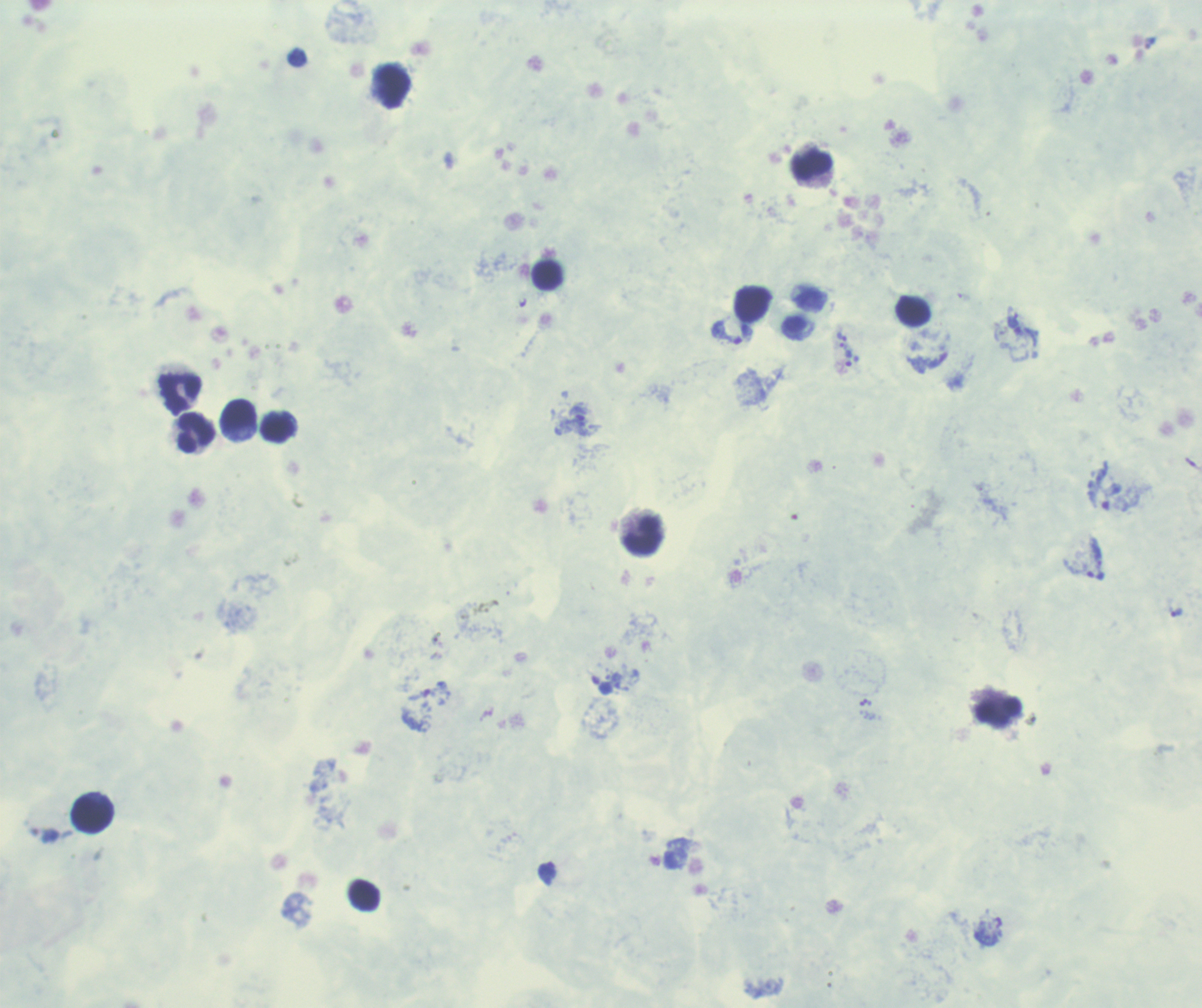
Approximate centers as (x, y) in pixels. Leukocyte locations: (393, 86), (812, 165), (548, 276), (753, 304), (914, 312), (180, 393), (239, 415), (277, 427), (196, 433), (643, 534), (998, 712), (91, 814), (364, 895). Trophozoite locations: (1014, 326), (727, 333), (842, 337), (849, 358), (579, 416), (1096, 575), (1176, 611), (602, 685), (547, 871). Background quality: poor. Image is 1202×1008 pixels. Romanowsky-stained preparation. Previously used in a real diagnosis. Result: positive for Plasmodium parasites. 100x magnification. One field from this slide. Thick blood smear.